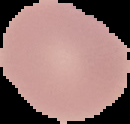

result = no Plasmodium parasites detected
image type = segmented cell region on a black background
preparation = thin blood film
image size = 130×124 pixels